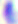
Summary:
  - Modality: photomicrograph
  - Identification: Toxoplasma gondii
  - Magnification: 400x